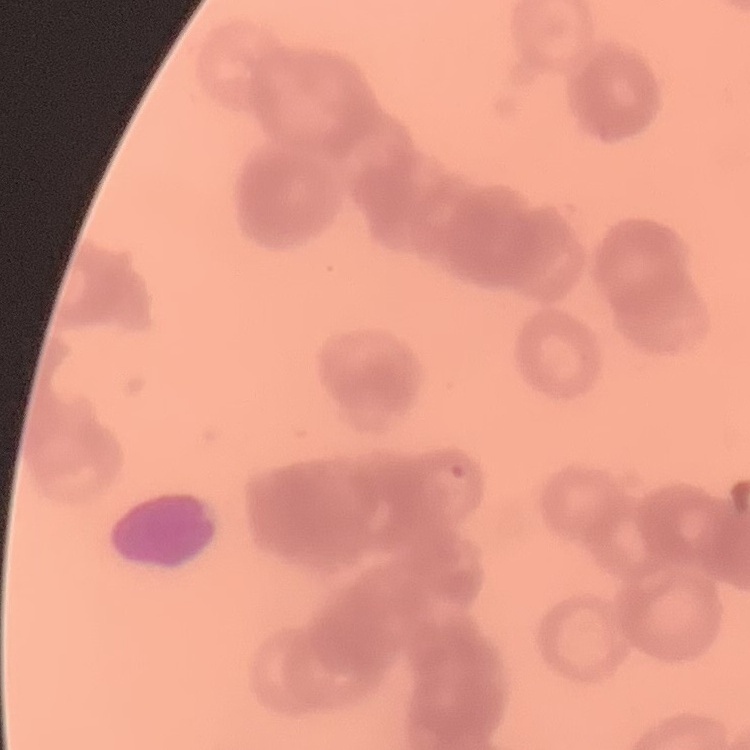

erythrocyte morphology = rouleaux formation
stain = Field's or Giemsa
image type = square crop of a larger photomicrograph
preparation = thin peripheral smear